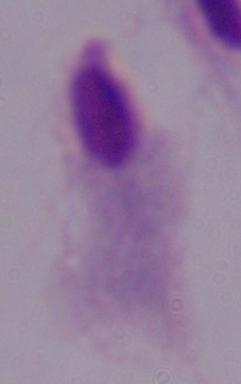

modality = photomicrograph
identification = trichomonad
magnification = 1000x